Report the malaria status of this cell.
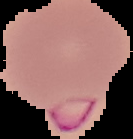

Parasitized.

The area outside the segmented cell region is set to black. Image is 133×139 pixels. From a thin blood film.